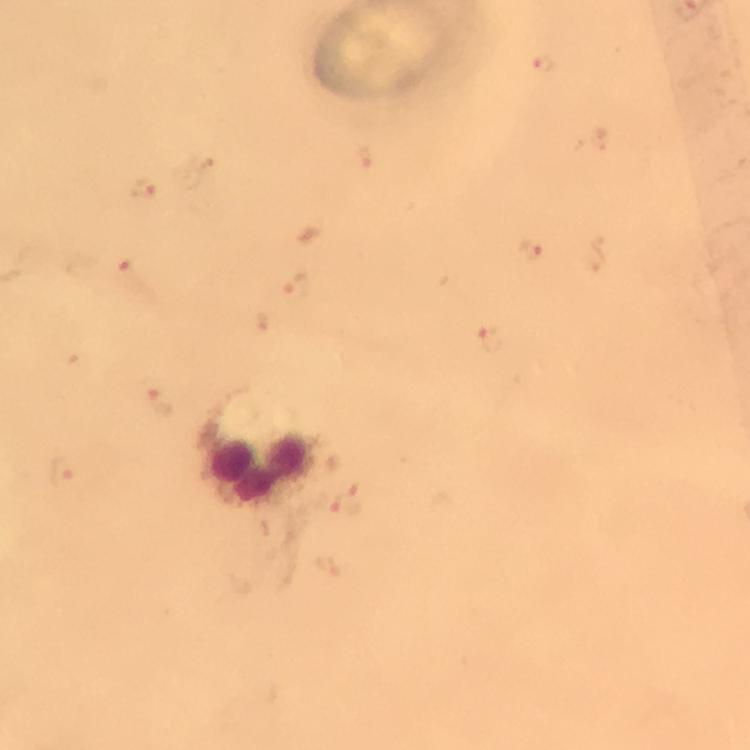
Approximate centers as (x, y) in pixels.
Summary:
  - Plasmodium parasite locations: (545, 64), (366, 158), (144, 188), (532, 249), (128, 267), (295, 286), (491, 340), (162, 403), (62, 473), (348, 500)
  - Leukocyte locations: (259, 470)
  - Preparation: thick smear
  - Stain: Giemsa
  - Image size: 750×750 pixels
  - Immersion oil: applied
  - Context: from a diagnostic examination for malaria
  - Cropped from: one field of view
  - Capture: smartphone camera through the microscope
  - Magnification: 100x